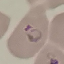 Malaria status: parasitized. Giemsa-stained preparation. Cell patch, automatically extracted from a larger field of view and resized to 64 × 64 pixels. Photographed with a smartphone camera at the microscope eyepiece. Thin blood smear.